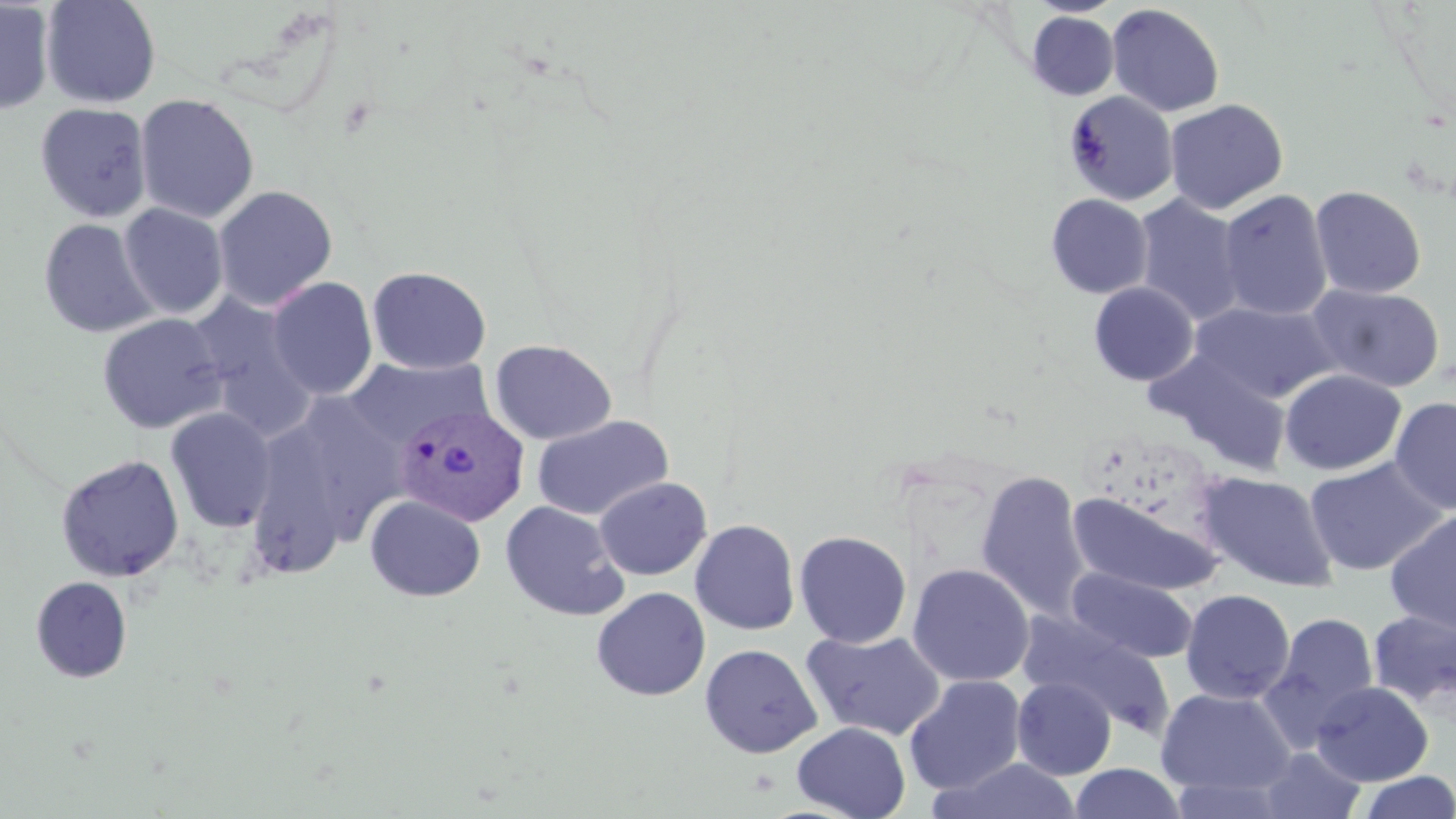
Summary:
  - Coordinate format: approximate bounding boxes as [x1, y1, x2, y2] in pixels
  - Uninfected red blood cell locations: [40, 0, 162, 109], [0, 1, 55, 114], [1026, 1, 1125, 18], [1107, 3, 1226, 117], [1026, 11, 1119, 100], [1064, 90, 1180, 206], [135, 93, 259, 223], [1164, 98, 1288, 215], [35, 102, 152, 223], [213, 185, 337, 311], [1310, 185, 1427, 299], [1217, 189, 1333, 322], [1046, 193, 1153, 298], [1132, 194, 1246, 325], [118, 203, 229, 319], [38, 218, 158, 338], [367, 266, 492, 375], [267, 277, 378, 400], [1088, 282, 1199, 385], [1307, 284, 1446, 393], [185, 291, 320, 441], [1191, 300, 1340, 404], [97, 313, 228, 434], [489, 339, 617, 445], [1149, 350, 1291, 474], [344, 356, 492, 448], [1279, 369, 1406, 476], [307, 391, 410, 540], [1389, 397, 1456, 516], [165, 407, 277, 532], [531, 414, 673, 521], [253, 425, 347, 586], [55, 454, 184, 583], [1305, 456, 1449, 577], [975, 469, 1091, 621], [1196, 472, 1340, 593], [593, 476, 712, 580], [1068, 491, 1224, 597], [365, 494, 486, 602], [499, 500, 629, 621], [1384, 509, 1456, 634], [690, 520, 800, 635], [794, 530, 912, 648], [907, 563, 1035, 686], [1067, 567, 1198, 663], [30, 576, 132, 683], [591, 587, 711, 701], [1180, 589, 1296, 704], [1367, 610, 1456, 710], [1265, 612, 1380, 732], [1019, 613, 1176, 737], [801, 629, 946, 741], [699, 643, 822, 758], [904, 675, 1027, 795], [1012, 677, 1116, 780], [1311, 681, 1433, 786], [1156, 688, 1296, 796], [792, 722, 910, 819], [1260, 747, 1367, 819], [930, 758, 1084, 818], [1069, 763, 1187, 819], [1357, 771, 1456, 818]
  - Plasmodium vivax-infected red blood cell locations: [394, 403, 529, 525]
  - Slide-level diagnosis: Plasmodium vivax
  - Modality: light microscopy
  - Magnification: 1000x
  - Field of view: single
  - Image size: 1456×819 pixels
  - Stain: May-Grünwald-Giemsa
  - Preparation: thin blood smear